Name the malaria species.
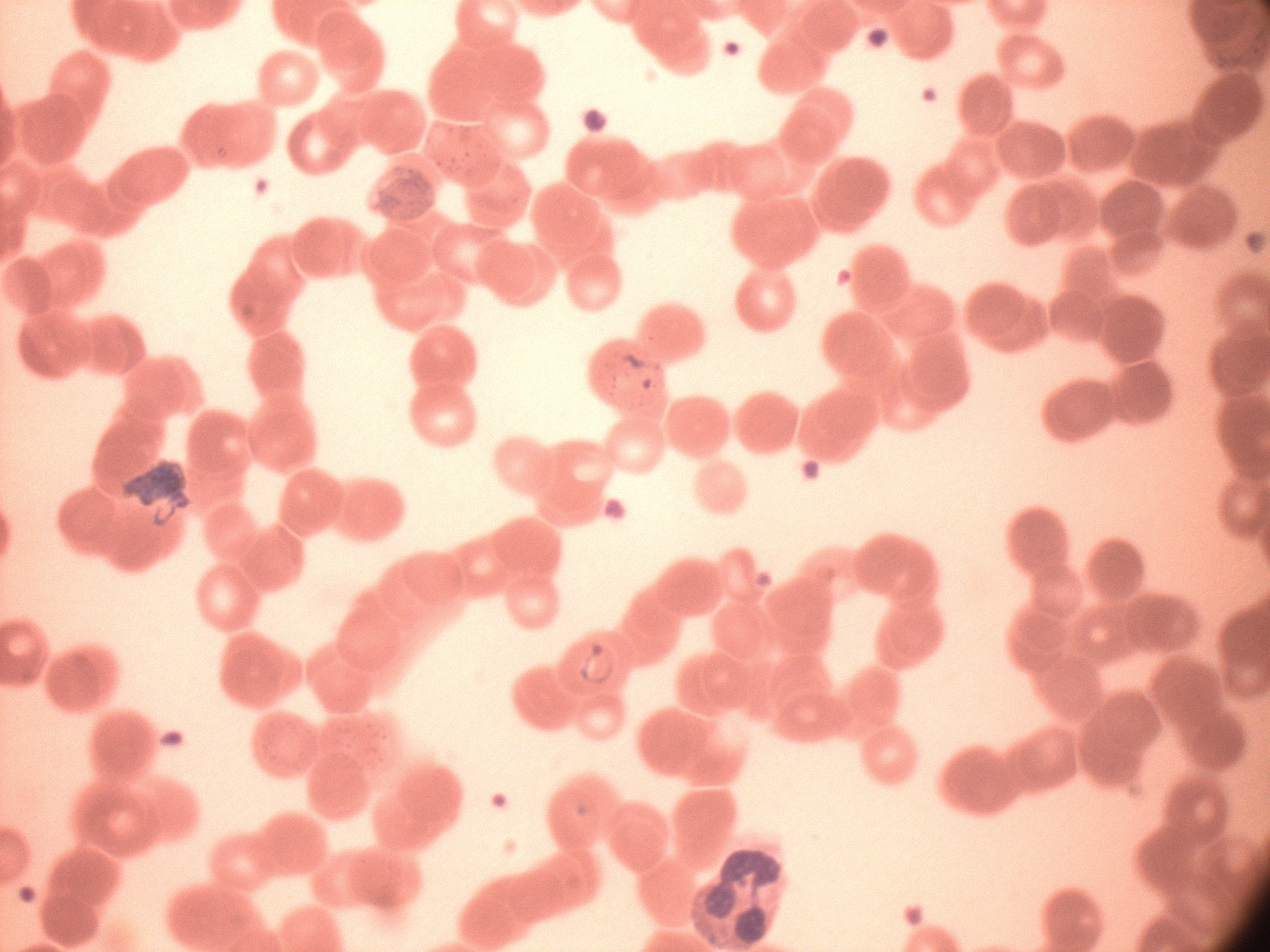
Plasmodium falciparum.

Approximate bounding boxes as named x1/y1/x2/y2 corners in pixels, from the source annotation, which is not necessarily exhaustive.
Summary:
  - Ring form locations: (x1=594, y1=342, x2=664, y2=403), (x1=566, y1=640, x2=626, y2=688)
  - Field of view: one from this slide
  - Preparation: thin blood film
  - Stain: Giemsa
  - Image size: 1270×952 pixels
  - Microscope: Leica DM2000 with built-in camera
  - Magnification: 100x